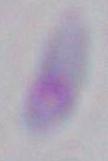
modality: micrograph
identification: Toxoplasma gondii
magnification: 1000x